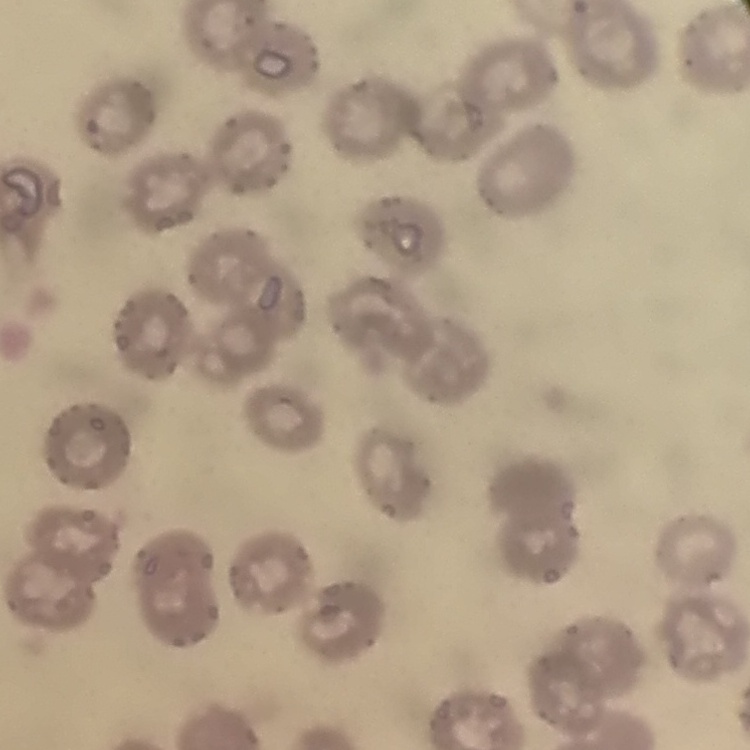
Summary:
  - Erythrocyte morphology: no rouleaux formation
  - Stain: Field's or Giemsa
  - Preparation: thin blood smear
  - Image type: square crop of a larger photomicrograph